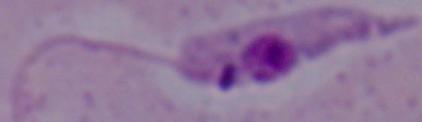

1000x magnification. Photomicrograph. A Leishmania parasite is shown.